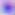
Summary:
  - Identification: Toxoplasma gondii
  - Magnification: 400x
  - Modality: photomicrograph